State the blood parasite species.
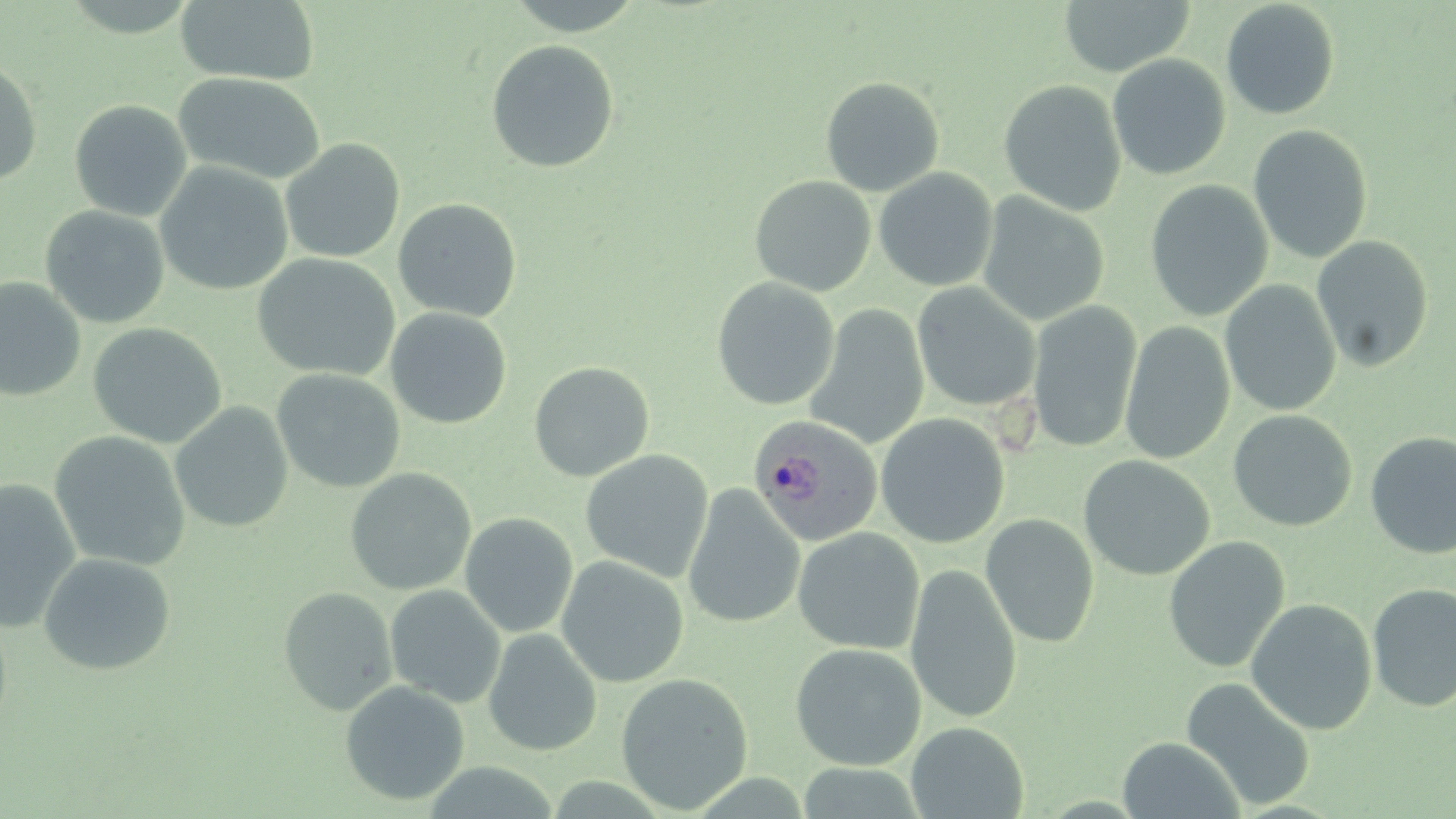

Plasmodium ovale.

{
  "image_size": "1456×819 pixels",
  "modality": "optical microscopy",
  "plasmodium_ovale_infected_red_blood_cell_locations": "approximate bounding boxes as (x1,y1)-(x2,y2) corner pairs in pixels: (748,415)-(882,546)",
  "stain": "May-Grünwald-Giemsa",
  "field_of_view": "single",
  "preparation": "thin blood film",
  "magnification": "1000x",
  "uninfected_red_blood_cell_locations": "approximate bounding boxes as (x1,y1)-(x2,y2) corner pairs in pixels: (175,0)-(321,86), (1058,0)-(1195,76), (1220,1)-(1340,120), (485,39)-(619,172), (1107,54)-(1230,180), (0,58)-(43,186), (172,72)-(326,185), (820,76)-(945,197), (999,79)-(1127,217), (68,99)-(192,221), (1248,124)-(1373,264), (281,139)-(405,263), (155,161)-(293,296), (873,168)-(998,292), (749,175)-(876,297), (1145,179)-(1273,321), (977,193)-(1109,326), (392,198)-(522,321), (39,205)-(170,329), (1312,235)-(1434,372), (252,253)-(400,381), (0,277)-(86,402), (712,277)-(840,411), (1220,279)-(1341,417), (912,283)-(1040,412), (1027,300)-(1143,453), (805,304)-(930,449), (385,307)-(512,429), (1120,321)-(1235,465), (88,323)-(227,448), (528,361)-(654,481), (271,369)-(406,494), (170,402)-(293,533), (1227,409)-(1357,532), (875,413)-(1010,548), (49,431)-(191,571), (1364,431)-(1456,559), (580,450)-(714,582), (1078,455)-(1215,580), (345,468)-(476,596), (0,480)-(81,634), (682,485)-(805,630), (460,512)-(578,638), (981,514)-(1100,648), (792,528)-(924,655), (1163,536)-(1290,673), (38,552)-(176,676), (556,555)-(689,688), (905,562)-(1023,724), (1367,582)-(1456,712), (385,584)-(506,708), (278,587)-(397,715), (1245,598)-(1378,735), (483,628)-(602,757), (789,643)-(926,770), (616,673)-(754,814), (1180,676)-(1316,811), (339,681)-(470,806), (906,722)-(1029,818), (1116,736)-(1246,818)"
}